Report the malaria status of this cell.
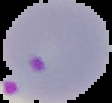

Parasitized.

image size = 112×103 pixels
image type = segmented cell region on a black background
preparation = thin blood film